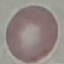
Summary:
  - Result: no malaria parasites seen
  - Stain: Giemsa
  - Image type: cell patch, automatically extracted from a larger field of view and resized to 64 × 64 pixels
  - Preparation: thin blood film
  - Capture: smartphone camera at the microscope eyepiece